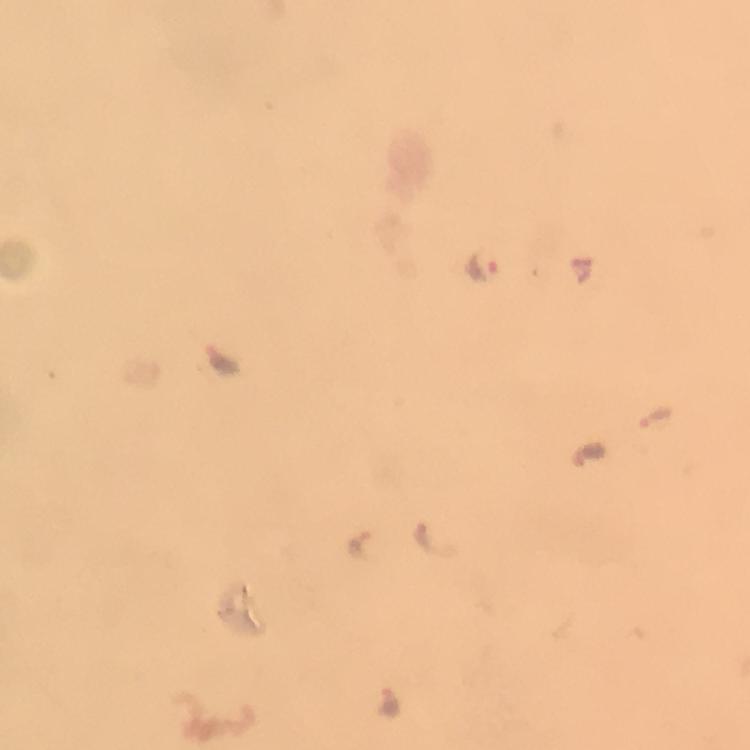

Approximate centers as [x, y] in pixels. Plasmodium parasite locations: [483, 264], [223, 360], [656, 416], [430, 540], [358, 546], [389, 704]. 100x magnification. Cropped region of a single field of view. Immersion oil applied. Thick smear. Giemsa stain. Photographed through the microscope with a smartphone camera. From a diagnostic examination for malaria. Image is 750×750 pixels.